Describe the morphology of the erythrocytes.
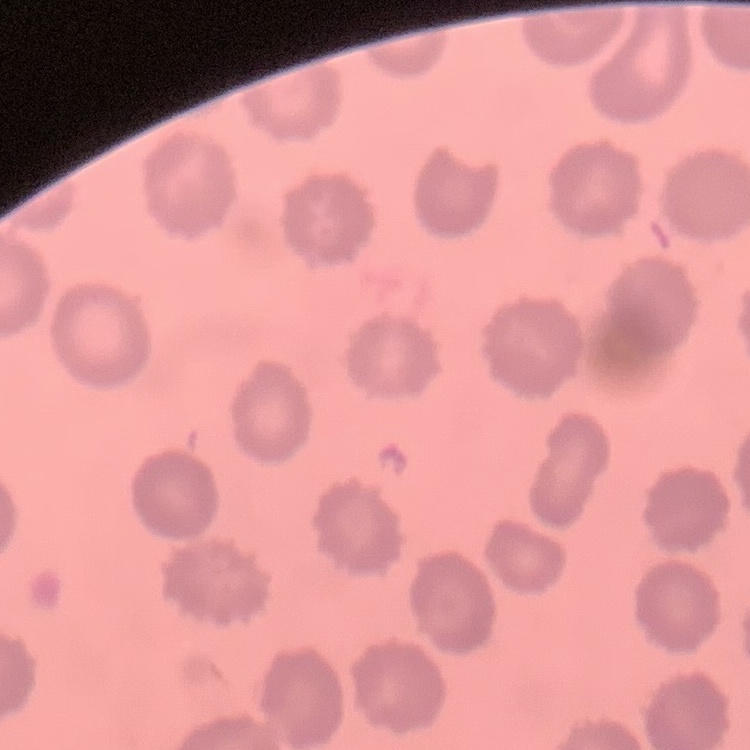
No rouleaux formation.

{
  "preparation": "thin blood smear",
  "image_type": "square crop of a larger photomicrograph",
  "stain": "Field's or Giemsa"
}